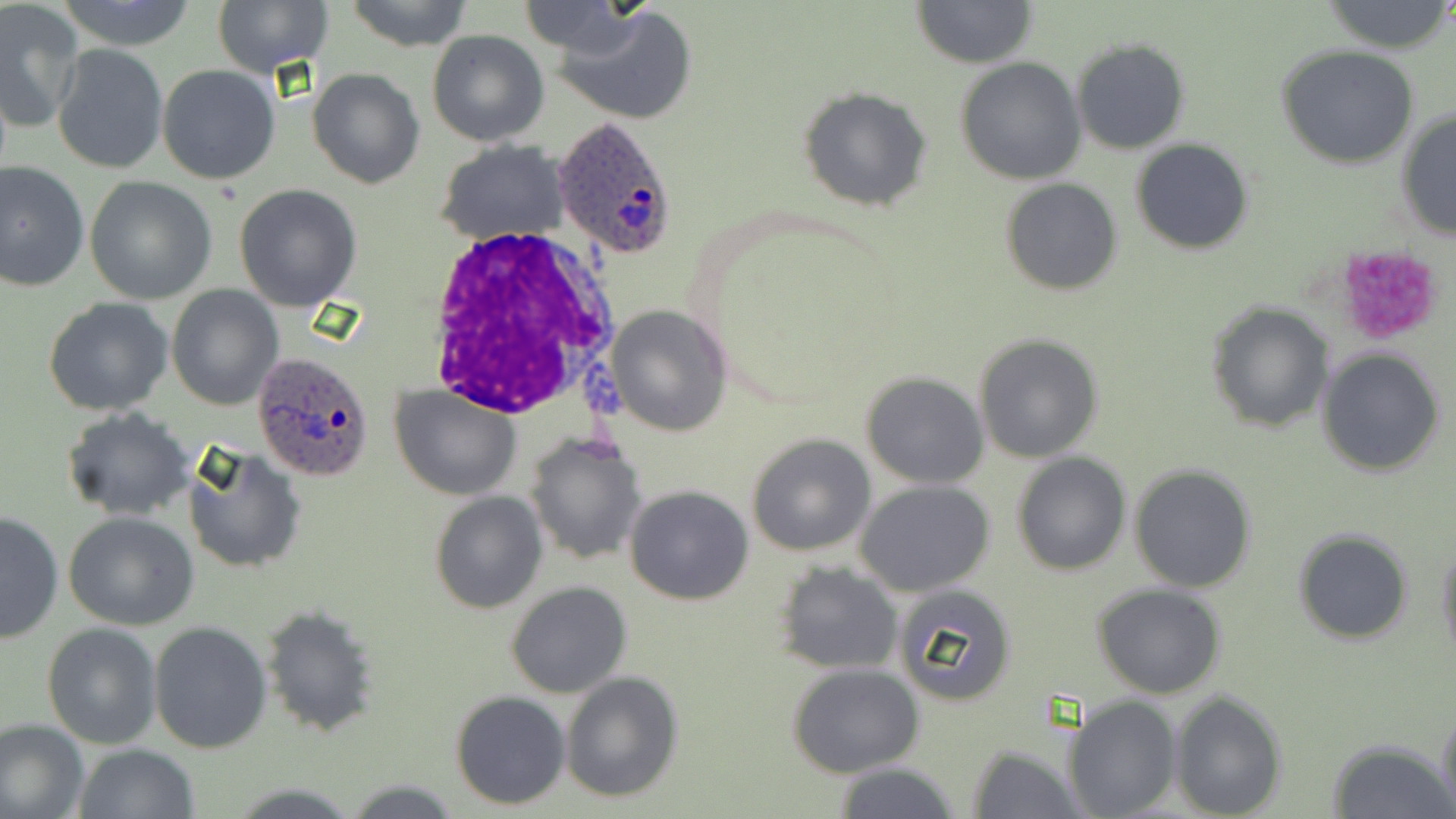

Summary:
  - Coordinate format: approximate bounding boxes as named x1/y1/x2/y2 corners in pixels
  - Plasmodium ovale-infected red blood cell locations: (x1=552, y1=118, x2=681, y2=263), (x1=254, y1=352, x2=376, y2=483)
  - Platelet locations: (x1=1334, y1=245, x2=1444, y2=345)
  - White blood cell locations: (x1=422, y1=226, x2=618, y2=419)
  - Uninfected red blood cell locations: (x1=56, y1=0, x2=200, y2=51), (x1=213, y1=0, x2=333, y2=76), (x1=344, y1=0, x2=475, y2=51), (x1=913, y1=0, x2=1036, y2=68), (x1=516, y1=2, x2=637, y2=55), (x1=1322, y1=2, x2=1451, y2=54), (x1=1, y1=4, x2=84, y2=130), (x1=558, y1=5, x2=697, y2=124), (x1=426, y1=29, x2=548, y2=146), (x1=1070, y1=37, x2=1191, y2=154), (x1=53, y1=43, x2=168, y2=176), (x1=1276, y1=44, x2=1421, y2=170), (x1=956, y1=57, x2=1086, y2=185), (x1=157, y1=64, x2=282, y2=185), (x1=309, y1=68, x2=425, y2=189), (x1=796, y1=86, x2=933, y2=213), (x1=1395, y1=109, x2=1455, y2=240), (x1=1130, y1=139, x2=1254, y2=255), (x1=434, y1=141, x2=569, y2=243), (x1=0, y1=159, x2=89, y2=291), (x1=85, y1=177, x2=218, y2=304), (x1=1000, y1=178, x2=1123, y2=296), (x1=234, y1=184, x2=362, y2=313), (x1=167, y1=286, x2=283, y2=410), (x1=43, y1=297, x2=173, y2=416), (x1=1204, y1=301, x2=1334, y2=434), (x1=605, y1=306, x2=731, y2=436), (x1=974, y1=333, x2=1105, y2=463), (x1=1317, y1=345, x2=1446, y2=477), (x1=862, y1=372, x2=989, y2=488), (x1=392, y1=384, x2=521, y2=499), (x1=63, y1=407, x2=196, y2=521), (x1=525, y1=433, x2=648, y2=564), (x1=745, y1=433, x2=876, y2=556), (x1=182, y1=444, x2=307, y2=575), (x1=1010, y1=454, x2=1131, y2=575), (x1=1129, y1=464, x2=1257, y2=592), (x1=856, y1=480, x2=995, y2=597), (x1=625, y1=485, x2=753, y2=605), (x1=429, y1=493, x2=547, y2=613), (x1=0, y1=511, x2=63, y2=645), (x1=63, y1=511, x2=200, y2=629), (x1=1292, y1=528, x2=1414, y2=644), (x1=1435, y1=538, x2=1456, y2=668), (x1=775, y1=562, x2=904, y2=675), (x1=505, y1=582, x2=632, y2=699), (x1=893, y1=583, x2=1019, y2=706), (x1=1092, y1=584, x2=1227, y2=699), (x1=259, y1=605, x2=380, y2=737), (x1=149, y1=622, x2=272, y2=752), (x1=42, y1=623, x2=162, y2=749), (x1=788, y1=663, x2=923, y2=777), (x1=559, y1=671, x2=684, y2=804), (x1=1170, y1=690, x2=1287, y2=819), (x1=450, y1=691, x2=570, y2=810), (x1=1066, y1=696, x2=1180, y2=819), (x1=1437, y1=703, x2=1456, y2=818), (x1=0, y1=719, x2=87, y2=819), (x1=1328, y1=737, x2=1450, y2=818), (x1=967, y1=742, x2=1087, y2=819), (x1=73, y1=745, x2=198, y2=819), (x1=832, y1=762, x2=963, y2=819), (x1=340, y1=778, x2=464, y2=817)
  - Slide-level diagnosis: Plasmodium ovale
  - Modality: optical microscopy
  - Magnification: 1000x
  - Preparation: thin blood film
  - Image size: 1456×819 pixels
  - Field of view: single
  - Stain: May-Grünwald-Giemsa